Classify this cell by malaria status.
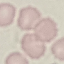
Uninfected.

stain: Giemsa
capture: smartphone camera at the microscope eyepiece
preparation: thin blood film
image_type: automatically extracted cell patch, resized to 64 × 64 pixels